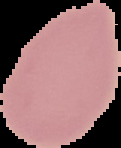
From a thin blood film. Malaria status: uninfected. The area outside the segmented cell region is set to black. Image is 121×148 pixels.